Locate every uninfected red blood cell.
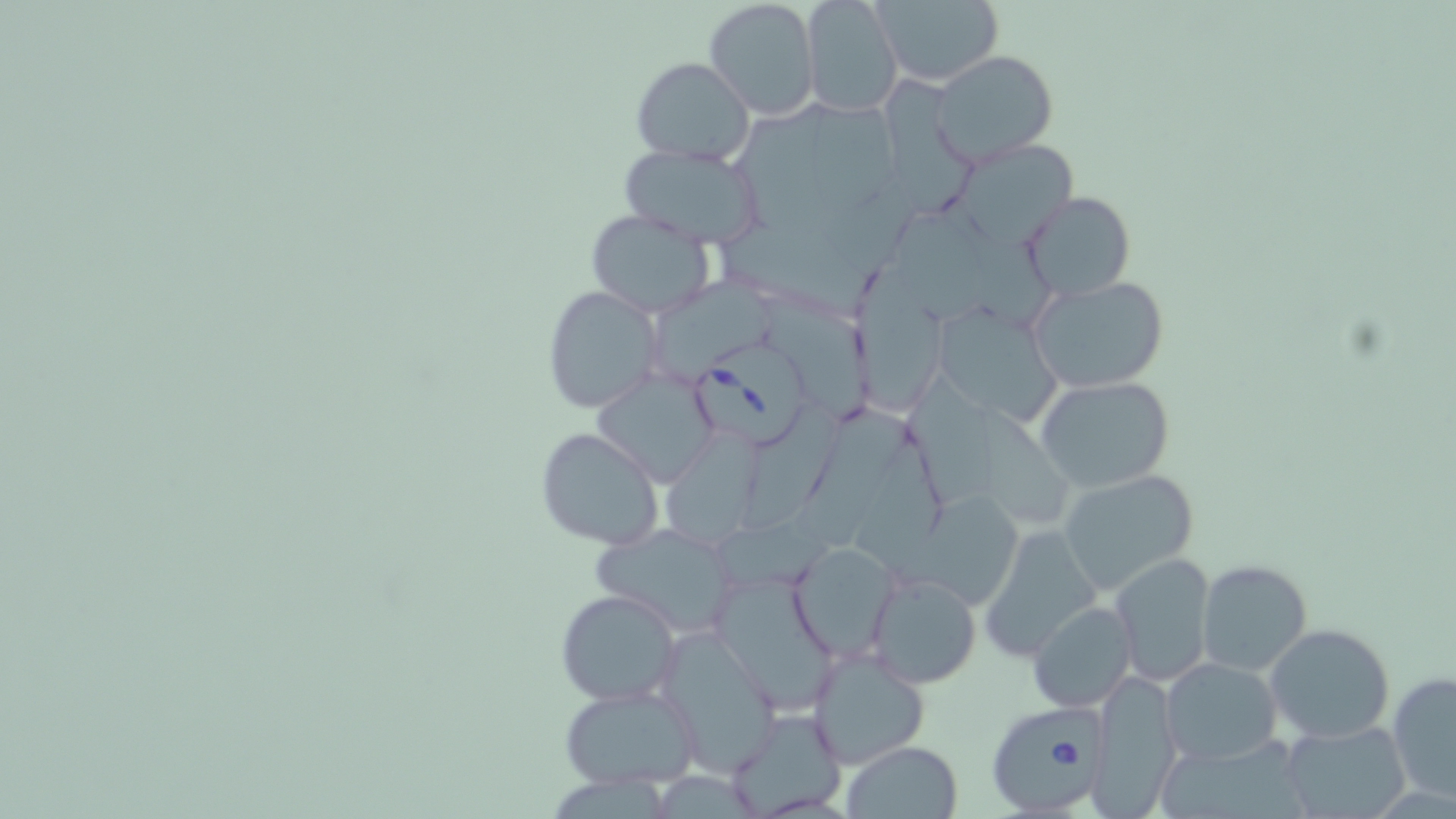
Approximate bounding boxes as (x1,y1)-(x2,y2) corner pairs in pixels.
Uninfected red blood cells: (704,0)-(821,120), (801,0)-(901,118), (873,0)-(1003,86), (931,50)-(1059,166), (631,56)-(754,166), (884,77)-(981,221), (962,141)-(1083,245), (618,142)-(766,247), (1023,191)-(1135,301), (585,207)-(715,318), (853,267)-(950,416), (652,273)-(778,385), (1027,274)-(1171,393), (542,284)-(664,415), (761,294)-(874,422), (930,303)-(1067,427), (592,369)-(719,487), (906,371)-(1001,509), (1035,376)-(1175,492), (797,403)-(914,556), (744,405)-(857,532), (981,407)-(1075,529), (862,424)-(948,568), (536,425)-(665,550), (664,436)-(759,549), (1058,469)-(1200,594), (905,488)-(1027,610), (591,523)-(742,639), (979,524)-(1106,662), (789,542)-(899,661), (1108,552)-(1217,687), (1196,560)-(1316,677), (864,569)-(982,689), (712,573)-(836,708), (555,589)-(681,707), (1027,601)-(1137,713), (1265,623)-(1395,744), (654,627)-(780,775), (805,647)-(931,769), (1161,658)-(1281,764), (1087,671)-(1183,816), (1388,672)-(1456,804), (556,683)-(703,790), (727,707)-(847,817), (1278,720)-(1410,819), (842,741)-(964,818).

slide-level diagnosis = Babesia divergens
stain = May-Grünwald-Giemsa
magnification = 1000x
preparation = thin blood smear
modality = light microscopy
Babesia divergens-infected red blood cell locations = approximate bounding boxes as (x1,y1)-(x2,y2) corner pairs in pixels: (694,345)-(812,452), (984,703)-(1104,813)
field of view = single
image size = 1456×819 pixels